Assess this cell for malaria.
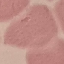
It is uninfected.

Photographed with a smartphone camera at the microscope eyepiece. Giemsa-stained preparation. Cell patch, automatically extracted from a larger field of view and resized to 64 × 64 pixels. Thin smear of blood.